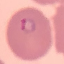

Summary:
  - Result: malaria parasites detected
  - Capture: smartphone camera at the microscope eyepiece
  - Stain: Giemsa
  - Image type: automatically extracted cell patch, resized to 64 × 64 pixels
  - Preparation: thin blood smear